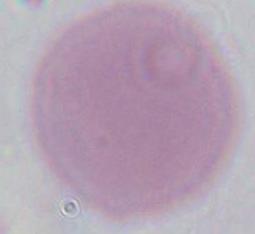
Photomicrograph. A red blood cell is seen. 1000x magnification.